Assess this cell for malaria.
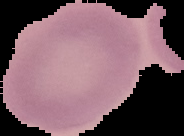

It is uninfected.

preparation = thin blood film
image size = 184×136 pixels
image type = segmented cell region on a black background